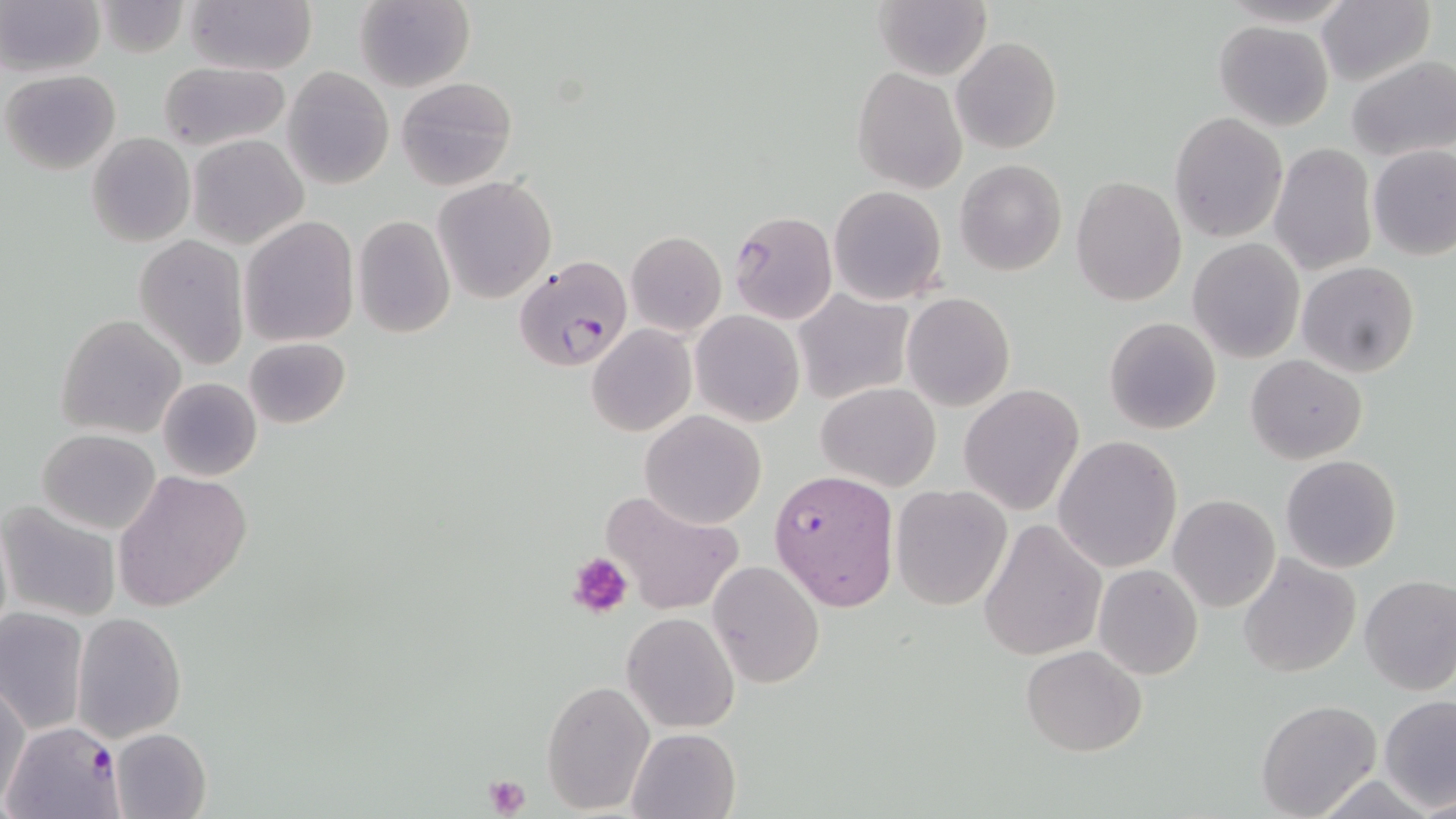

slide-level diagnosis = Plasmodium falciparum
platelet locations = approximate bounding boxes as (x1,y1)-(x2,y2) corner pairs in pixels: (568,553)-(633,619), (481,775)-(532,818)
uninfected red blood cell locations = approximate bounding boxes as (x1,y1)-(x2,y2) corner pairs in pixels: (0,0)-(104,78), (182,0)-(317,75), (353,0)-(476,92), (1316,0)-(1434,87), (95,1)-(189,57), (875,2)-(991,80), (1214,20)-(1334,131), (952,36)-(1061,154), (1345,55)-(1454,163), (159,61)-(288,150), (852,66)-(967,194), (283,67)-(392,189), (2,69)-(120,175), (395,76)-(517,191), (1170,112)-(1288,243), (87,132)-(195,247), (187,133)-(309,250), (1268,143)-(1377,276), (1369,145)-(1456,261), (954,160)-(1067,276), (433,176)-(558,304), (1070,176)-(1187,306), (828,185)-(947,305), (727,209)-(838,323), (353,214)-(455,340), (239,216)-(360,346), (626,231)-(726,336), (133,234)-(249,370), (1188,238)-(1304,363), (1296,262)-(1420,379), (74,263)-(221,420), (794,290)-(913,402), (901,292)-(1014,411), (690,311)-(805,427), (55,314)-(186,439), (1103,316)-(1222,435), (587,324)-(696,438), (243,337)-(351,428), (1246,355)-(1367,464), (156,377)-(262,481), (817,382)-(942,491), (959,384)-(1085,517), (640,410)-(768,528), (38,428)-(161,533), (1053,436)-(1184,574), (1280,454)-(1402,574), (111,469)-(253,612), (890,483)-(1013,611), (599,488)-(745,616), (1168,495)-(1280,613), (2,501)-(120,621), (979,517)-(1107,662), (1237,555)-(1361,677), (709,559)-(825,688), (1094,565)-(1204,680), (1359,575)-(1456,694), (0,610)-(87,734), (73,612)-(188,742), (622,612)-(739,731), (1021,644)-(1148,756), (540,678)-(655,814), (1,682)-(30,810), (1378,695)-(1456,811), (1256,699)-(1382,818), (627,727)-(741,819), (111,728)-(212,818)
magnification = 1000x
modality = optical microscopy
Plasmodium falciparum-infected red blood cell locations = approximate bounding boxes as (x1,y1)-(x2,y2) corner pairs in pixels: (512,253)-(631,371), (768,469)-(898,614), (6,719)-(123,817)
preparation = thin blood film
field of view = one of a larger specimen
image size = 1456×819 pixels
stain = May-Grünwald-Giemsa